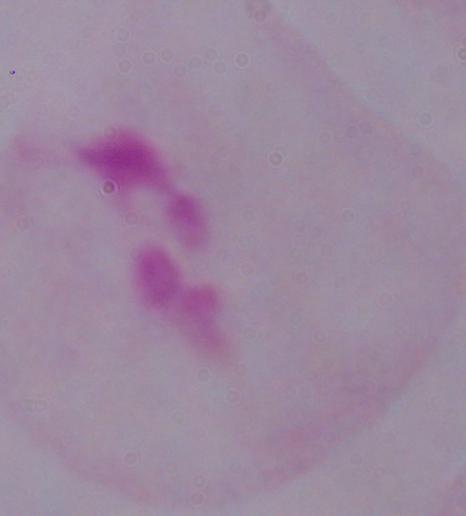

Summary:
  - Magnification: 1000x
  - Modality: micrograph
  - Identification: trichomonad